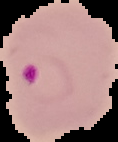 Result: Plasmodium parasites identified. Cell region segmented out of the field of view; the surrounding area is masked to black. Image is 118×142 pixels. From a thin blood film.